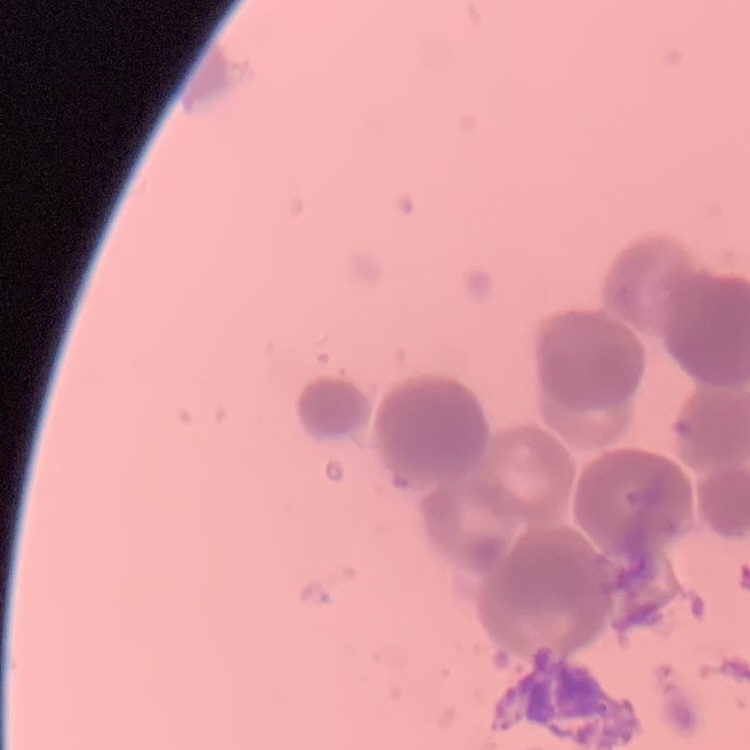

The erythrocytes show rouleaux formation. Thin blood smear. Square crop of a larger photomicrograph. Stained with either Field's or Giemsa.